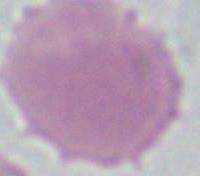

Summary:
  - Modality: photomicrograph
  - Magnification: 1000x
  - Identification: erythrocyte